Report the malaria status of this cell.
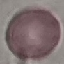

Uninfected.

{
  "capture": "smartphone camera at the microscope eyepiece",
  "image_type": "cell patch, automatically extracted from a larger field of view and resized to 64 × 64 pixels",
  "stain": "Giemsa",
  "preparation": "thin blood smear"
}